Give the preparation type.
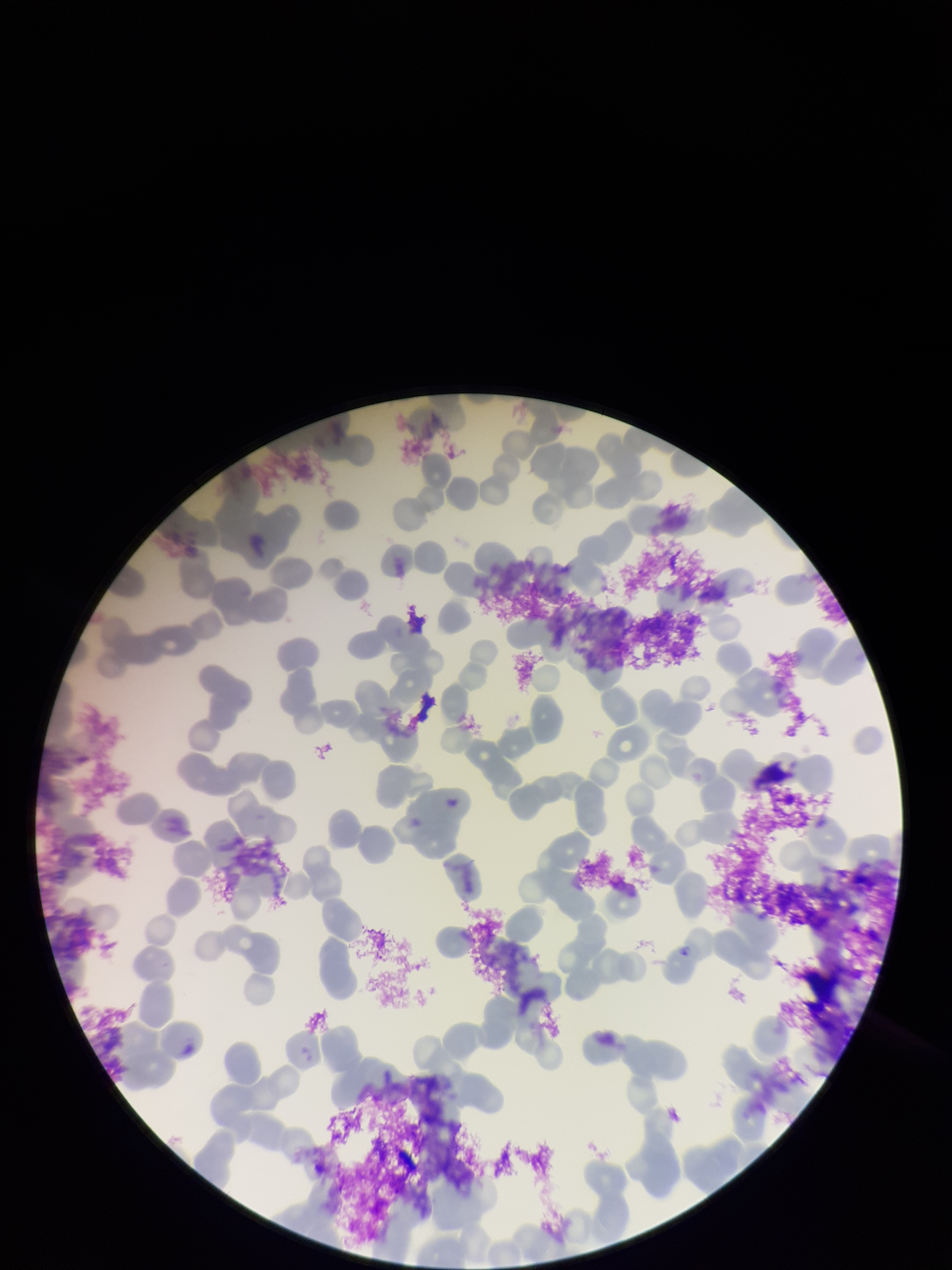

Thin.

Summary:
  - Capture: smartphone photograph through the microscope eyepiece
  - Parasitized red blood cell count: 0
  - Field of view: single
  - Parasitized red blood cells: none detected
  - Patient malaria status: positive
  - Image size: 952×1270 pixels
  - Species reported for this patient: Plasmodium falciparum
  - Stain: Giemsa
  - Red blood cell count: 149